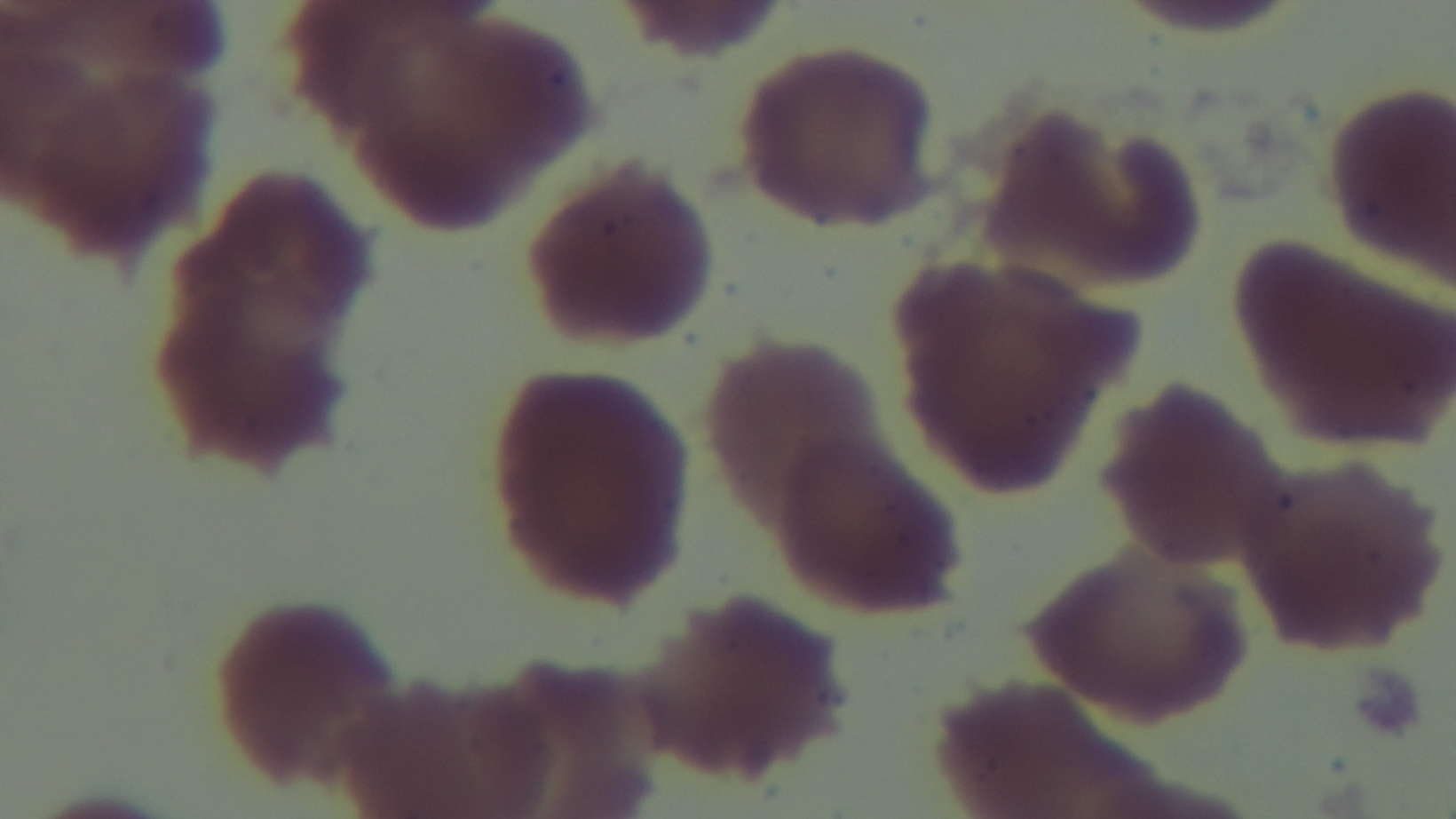

{
  "field_of_view": "single",
  "stain": "Giemsa",
  "malaria_status": "negative",
  "preparation": "thin smear",
  "modality": "light microscopy",
  "capture": "mounted 4K digital camera",
  "objective": "100x oil immersion"
}